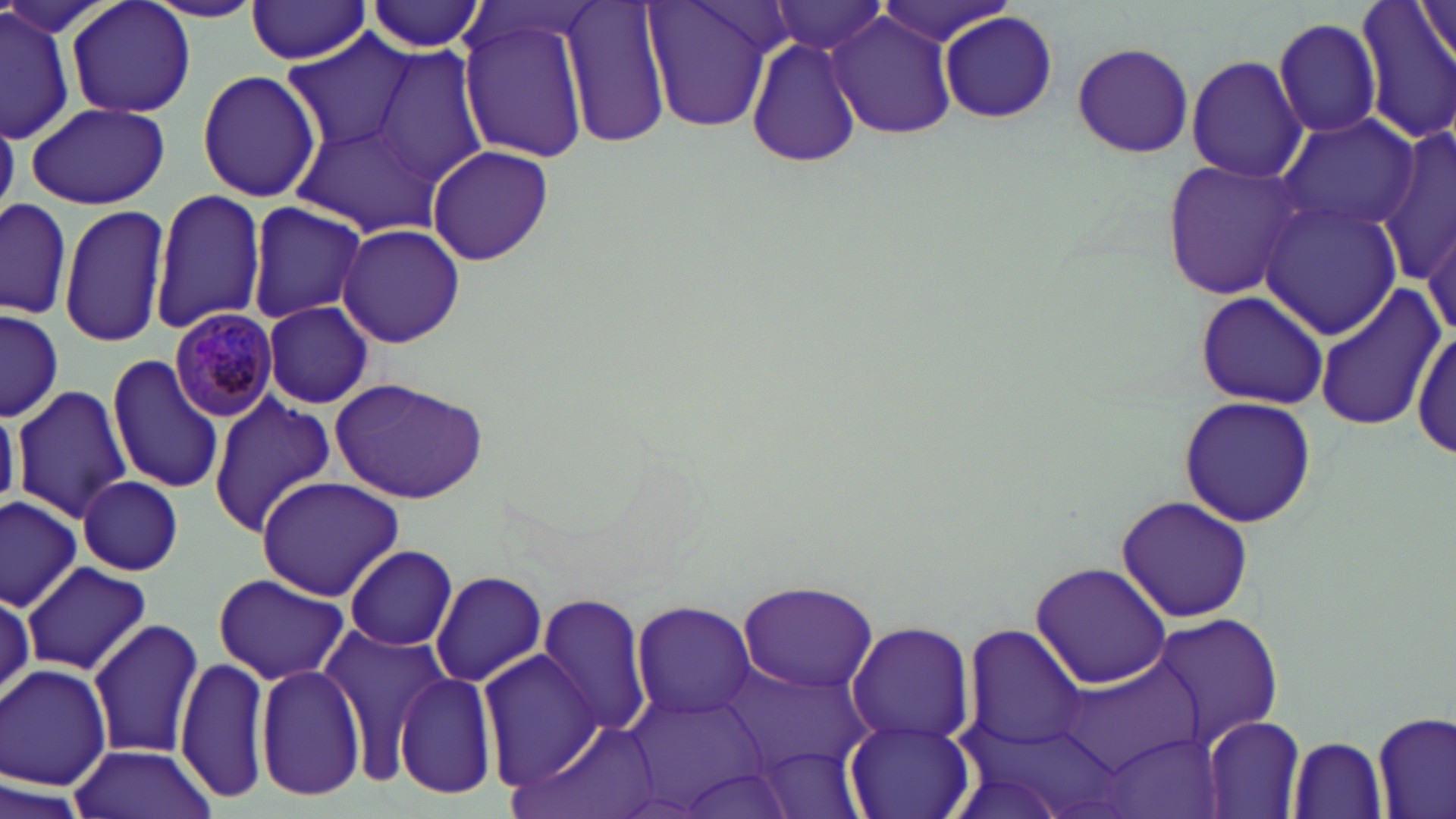

slide_level_diagnosis: Plasmodium malariae
field_of_view: single
stain: May-Grünwald-Giemsa
modality: light microscopy
plasmodium_malariae_infected_red_blood_cell_locations: 'approximate bounding boxes as [x1, y1, x2, y2] in pixels: [170, 306, 278, 422]'
preparation: thin blood smear
uninfected_red_blood_cell_locations: 'approximate bounding boxes as [x1, y1, x2, y2] in pixels: [67, 0, 195, 119], [148, 0, 266, 23], [558, 0, 671, 149], [643, 0, 785, 133], [1356, 0, 1456, 144], [365, 1, 485, 53], [766, 1, 893, 58], [873, 1, 1017, 48], [1416, 1, 1455, 70], [245, 2, 371, 64], [0, 4, 77, 144], [938, 11, 1058, 125], [829, 13, 958, 139], [457, 15, 592, 164], [1273, 15, 1383, 138], [744, 32, 865, 171], [283, 33, 417, 156], [1069, 41, 1197, 159], [374, 49, 488, 185], [1185, 54, 1307, 181], [197, 68, 321, 204], [26, 101, 169, 209], [1275, 111, 1422, 234], [298, 120, 443, 237], [1379, 123, 1456, 294], [426, 145, 554, 265], [1158, 156, 1307, 301], [149, 189, 266, 333], [0, 197, 74, 320], [1259, 200, 1404, 339], [245, 202, 369, 323], [59, 203, 172, 347], [1421, 206, 1456, 350], [1285, 220, 1430, 399], [337, 223, 466, 348], [1313, 286, 1442, 431], [1193, 288, 1328, 409], [261, 301, 373, 409], [1, 307, 64, 422], [1408, 324, 1456, 462], [107, 354, 226, 496], [330, 377, 490, 502], [11, 385, 133, 523], [209, 393, 335, 537], [1177, 395, 1318, 527], [77, 477, 185, 573], [256, 478, 404, 600], [1114, 495, 1256, 623], [0, 496, 82, 607], [343, 545, 459, 651], [1029, 559, 1174, 690], [22, 561, 150, 676], [430, 571, 548, 686], [212, 575, 352, 685], [735, 578, 881, 696], [0, 589, 34, 705], [533, 592, 656, 735], [631, 600, 757, 720], [1141, 611, 1287, 749], [89, 618, 204, 762], [846, 620, 975, 747], [320, 622, 450, 777], [964, 624, 1088, 752], [479, 645, 598, 784], [1060, 651, 1209, 774], [176, 654, 273, 805], [722, 659, 873, 780], [1, 664, 113, 791], [256, 664, 367, 800], [393, 672, 501, 800], [629, 691, 771, 812], [1373, 712, 1455, 818], [519, 717, 661, 819], [1200, 717, 1305, 818], [844, 720, 973, 819], [1098, 732, 1226, 819], [1288, 735, 1387, 818], [67, 744, 218, 819], [2, 771, 90, 819]'
magnification: 1000x
image_size: 1456×819 pixels